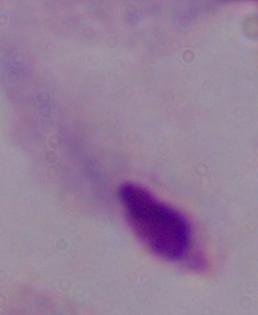

identification = trichomonad
magnification = 1000x
modality = photomicrograph